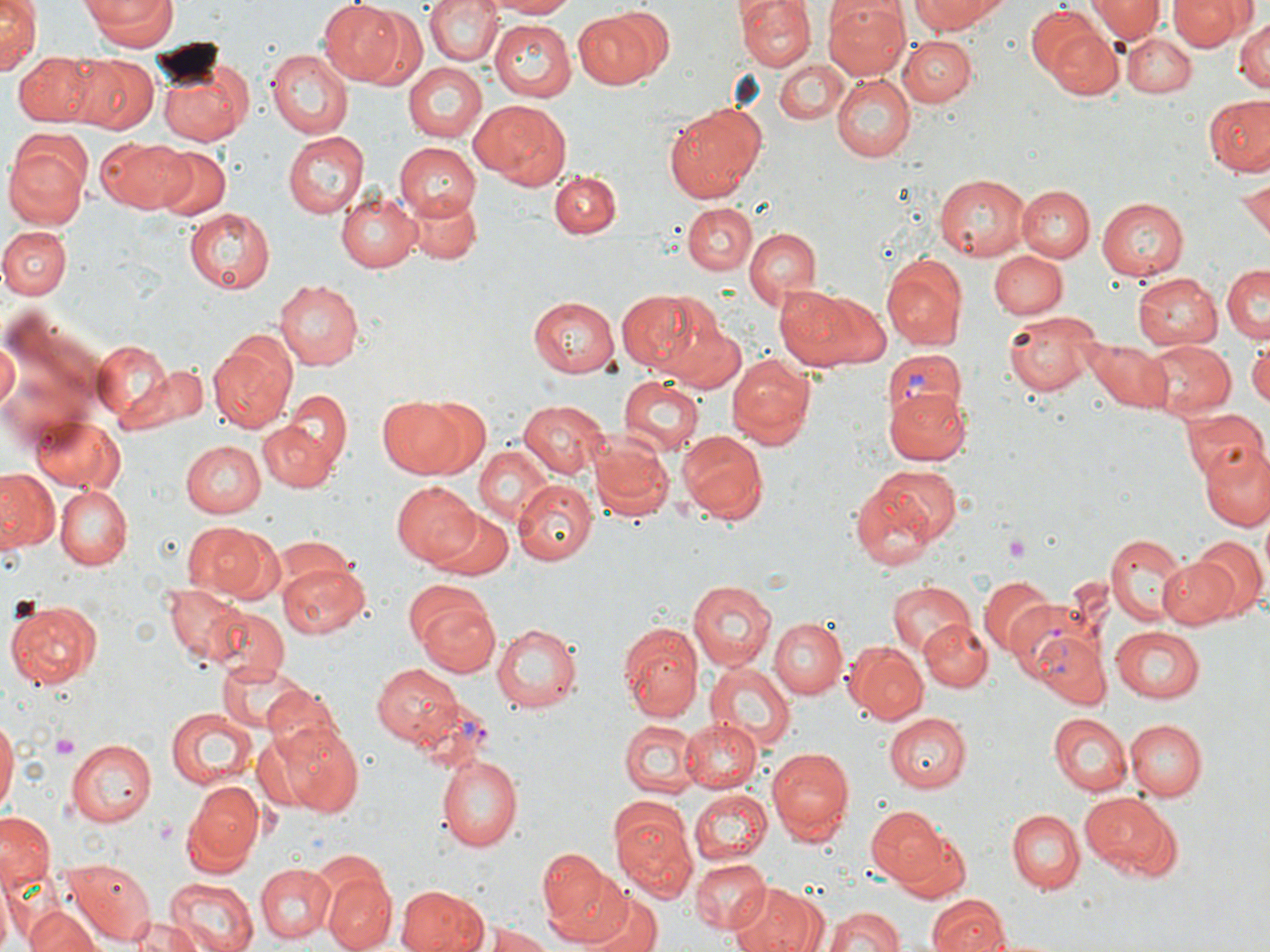
Summary:
  - Coordinate format: approximate bounding boxes as named x1/y1/x2/y2 corners in pixels
  - Uninfected red blood cell locations: (x1=0, y1=0, x2=41, y2=75), (x1=81, y1=0, x2=176, y2=50), (x1=425, y1=0, x2=502, y2=66), (x1=483, y1=0, x2=580, y2=19), (x1=739, y1=0, x2=813, y2=70), (x1=910, y1=0, x2=1009, y2=37), (x1=1086, y1=0, x2=1163, y2=43), (x1=1168, y1=0, x2=1246, y2=51), (x1=317, y1=1, x2=404, y2=85), (x1=822, y1=1, x2=908, y2=80), (x1=1202, y1=2, x2=1267, y2=69), (x1=1027, y1=5, x2=1111, y2=82), (x1=349, y1=6, x2=429, y2=92), (x1=569, y1=8, x2=667, y2=94), (x1=1233, y1=16, x2=1268, y2=94), (x1=489, y1=18, x2=574, y2=100), (x1=1044, y1=25, x2=1124, y2=99), (x1=1125, y1=34, x2=1195, y2=98), (x1=899, y1=36, x2=975, y2=106), (x1=263, y1=49, x2=353, y2=140), (x1=18, y1=52, x2=102, y2=128), (x1=68, y1=55, x2=158, y2=133), (x1=775, y1=60, x2=846, y2=127), (x1=401, y1=61, x2=487, y2=144), (x1=156, y1=63, x2=250, y2=146), (x1=833, y1=74, x2=913, y2=163), (x1=1205, y1=96, x2=1270, y2=174), (x1=471, y1=99, x2=572, y2=189), (x1=664, y1=107, x2=764, y2=202), (x1=282, y1=131, x2=367, y2=217), (x1=97, y1=139, x2=196, y2=213), (x1=4, y1=143, x2=90, y2=231), (x1=393, y1=143, x2=483, y2=220), (x1=155, y1=145, x2=231, y2=220), (x1=549, y1=168, x2=624, y2=244), (x1=932, y1=172, x2=1033, y2=262), (x1=1239, y1=179, x2=1269, y2=243), (x1=1015, y1=185, x2=1093, y2=262), (x1=333, y1=189, x2=422, y2=272), (x1=401, y1=189, x2=481, y2=265), (x1=1097, y1=197, x2=1188, y2=280), (x1=682, y1=203, x2=758, y2=276), (x1=183, y1=208, x2=274, y2=293), (x1=2, y1=226, x2=72, y2=301), (x1=743, y1=226, x2=821, y2=309), (x1=990, y1=248, x2=1066, y2=320), (x1=881, y1=253, x2=969, y2=349), (x1=1222, y1=262, x2=1270, y2=340), (x1=1132, y1=271, x2=1223, y2=347), (x1=277, y1=277, x2=366, y2=369), (x1=773, y1=285, x2=866, y2=370), (x1=619, y1=288, x2=724, y2=381), (x1=816, y1=293, x2=893, y2=366), (x1=528, y1=296, x2=618, y2=377), (x1=1002, y1=316, x2=1099, y2=394), (x1=663, y1=318, x2=745, y2=392), (x1=0, y1=336, x2=19, y2=412), (x1=91, y1=339, x2=177, y2=424), (x1=1145, y1=341, x2=1232, y2=420), (x1=1248, y1=342, x2=1270, y2=412), (x1=208, y1=343, x2=298, y2=432), (x1=1090, y1=344, x2=1173, y2=409), (x1=726, y1=356, x2=814, y2=448), (x1=149, y1=364, x2=207, y2=425), (x1=618, y1=376, x2=700, y2=458), (x1=883, y1=386, x2=971, y2=466), (x1=283, y1=389, x2=354, y2=470), (x1=376, y1=395, x2=469, y2=479), (x1=419, y1=399, x2=490, y2=476), (x1=518, y1=400, x2=610, y2=478), (x1=1182, y1=406, x2=1266, y2=486), (x1=28, y1=415, x2=127, y2=493), (x1=259, y1=420, x2=334, y2=493), (x1=677, y1=430, x2=766, y2=519), (x1=589, y1=437, x2=672, y2=522), (x1=1200, y1=438, x2=1270, y2=530), (x1=181, y1=440, x2=264, y2=518), (x1=473, y1=445, x2=556, y2=526), (x1=0, y1=468, x2=57, y2=551), (x1=851, y1=470, x2=955, y2=572), (x1=392, y1=479, x2=480, y2=566), (x1=515, y1=481, x2=597, y2=565), (x1=55, y1=485, x2=131, y2=568), (x1=427, y1=509, x2=514, y2=580), (x1=182, y1=521, x2=267, y2=600), (x1=1106, y1=531, x2=1192, y2=627), (x1=270, y1=535, x2=358, y2=595), (x1=1188, y1=535, x2=1267, y2=622), (x1=1157, y1=557, x2=1243, y2=629), (x1=278, y1=561, x2=368, y2=638), (x1=976, y1=573, x2=1060, y2=658), (x1=884, y1=578, x2=975, y2=659), (x1=403, y1=580, x2=491, y2=654), (x1=687, y1=580, x2=775, y2=671), (x1=161, y1=581, x2=245, y2=666), (x1=8, y1=598, x2=102, y2=688), (x1=419, y1=600, x2=499, y2=676), (x1=203, y1=605, x2=290, y2=685), (x1=767, y1=617, x2=845, y2=699), (x1=920, y1=620, x2=993, y2=693), (x1=492, y1=621, x2=585, y2=714), (x1=1023, y1=621, x2=1112, y2=711), (x1=620, y1=624, x2=702, y2=724), (x1=1108, y1=625, x2=1205, y2=704), (x1=843, y1=641, x2=929, y2=723), (x1=213, y1=659, x2=310, y2=735), (x1=707, y1=663, x2=795, y2=752), (x1=373, y1=665, x2=462, y2=747), (x1=263, y1=687, x2=345, y2=761), (x1=164, y1=707, x2=257, y2=790), (x1=884, y1=713, x2=971, y2=792), (x1=1047, y1=713, x2=1130, y2=795), (x1=678, y1=716, x2=762, y2=792), (x1=1126, y1=717, x2=1207, y2=799), (x1=0, y1=718, x2=17, y2=813), (x1=255, y1=719, x2=364, y2=817), (x1=617, y1=719, x2=699, y2=799), (x1=69, y1=737, x2=157, y2=827), (x1=766, y1=746, x2=855, y2=844), (x1=436, y1=754, x2=523, y2=852), (x1=188, y1=782, x2=263, y2=863), (x1=689, y1=790, x2=771, y2=865), (x1=1081, y1=792, x2=1179, y2=876), (x1=611, y1=804, x2=699, y2=900), (x1=867, y1=806, x2=950, y2=889), (x1=1007, y1=809, x2=1082, y2=893), (x1=0, y1=811, x2=54, y2=890), (x1=889, y1=823, x2=973, y2=902), (x1=539, y1=853, x2=630, y2=944), (x1=65, y1=857, x2=156, y2=943), (x1=691, y1=858, x2=771, y2=932), (x1=254, y1=862, x2=334, y2=943), (x1=0, y1=869, x2=20, y2=952), (x1=322, y1=874, x2=395, y2=952), (x1=164, y1=878, x2=256, y2=952), (x1=732, y1=882, x2=824, y2=952), (x1=394, y1=884, x2=490, y2=952), (x1=585, y1=891, x2=663, y2=952), (x1=928, y1=893, x2=1009, y2=951), (x1=822, y1=904, x2=908, y2=952), (x1=23, y1=905, x2=101, y2=952), (x1=122, y1=918, x2=205, y2=952), (x1=486, y1=924, x2=555, y2=951)
  - Plasmodium vivax-infected red blood cell locations: (x1=882, y1=351, x2=968, y2=428), (x1=1002, y1=590, x2=1098, y2=687), (x1=416, y1=703, x2=496, y2=775)
  - Platelet locations: (x1=1003, y1=532, x2=1030, y2=563), (x1=51, y1=732, x2=80, y2=760), (x1=152, y1=818, x2=177, y2=843)
  - Slide-level diagnosis: Plasmodium vivax
  - Field of view: single
  - Modality: optical microscopy
  - Magnification: 1000x
  - Preparation: thin blood smear
  - Stain: May-Grünwald-Giemsa
  - Image size: 1270×952 pixels